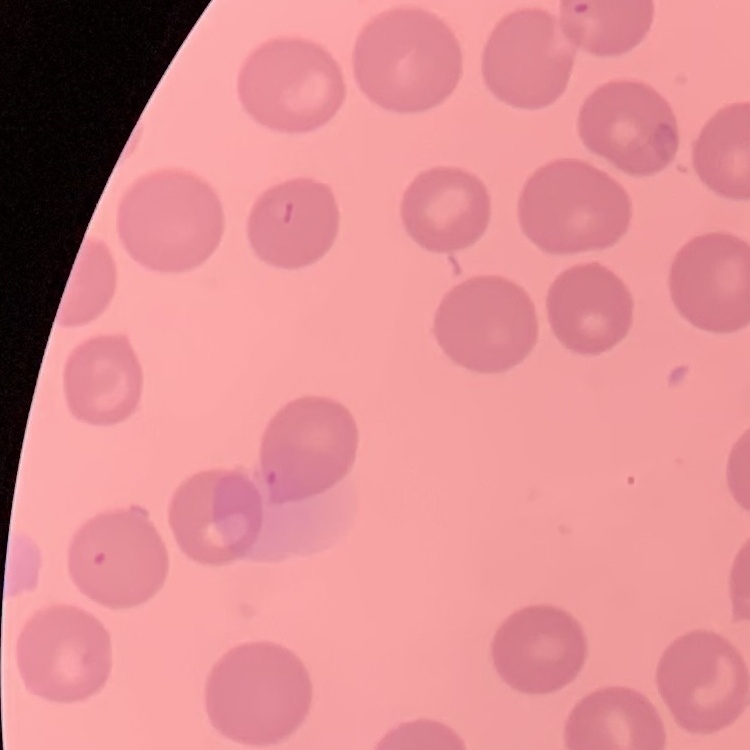

The red blood cells show no rouleaux formation. Square crop of a larger photomicrograph. Stained with either Field's or Giemsa. Thin blood film.